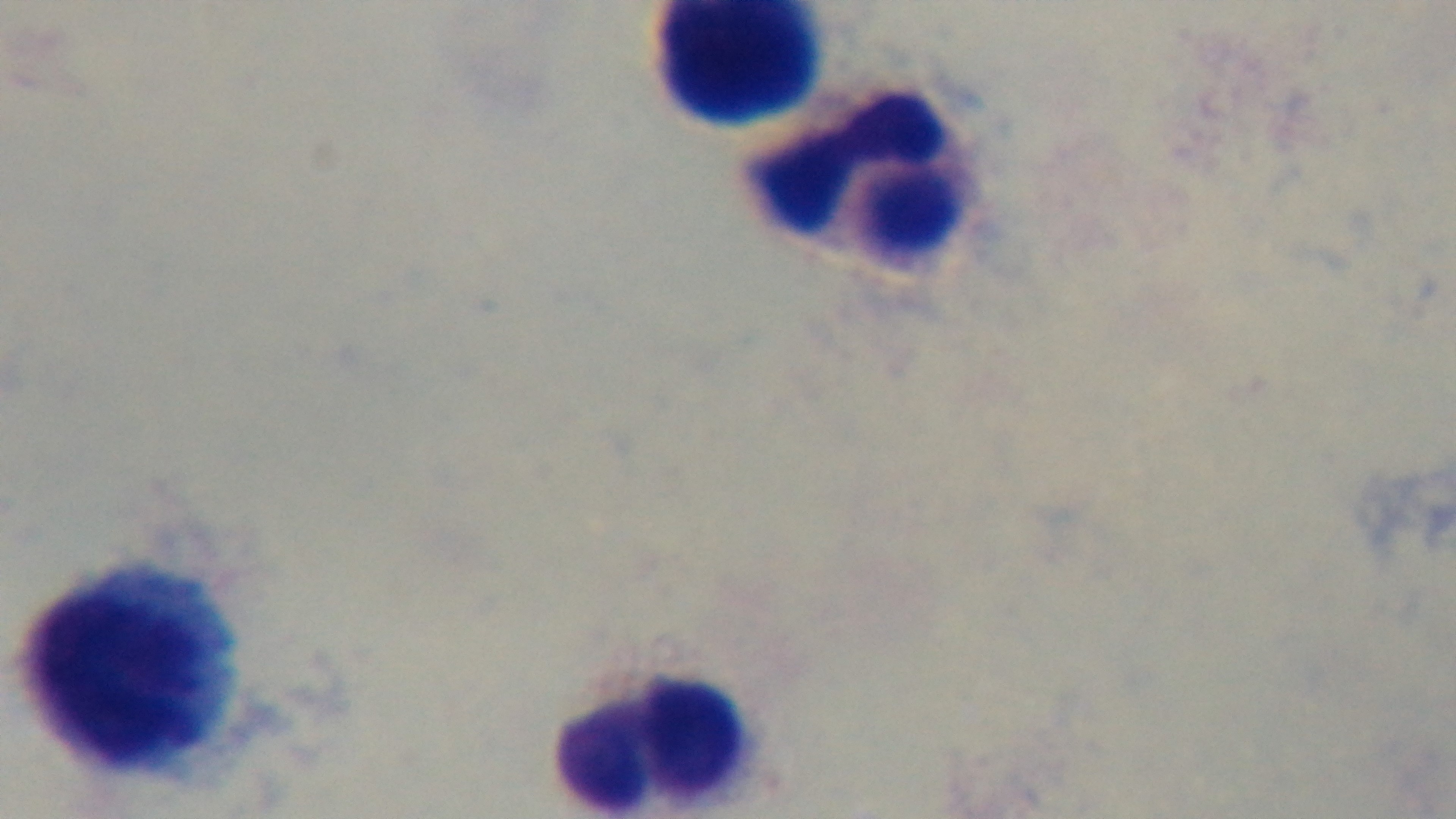
modality: light microscopy
capture: mounted 4K digital camera
preparation: thick smear
objective: 100x oil immersion
malaria_status: negative
field_of_view: single
stain: Giemsa